Name the blood parasite species.
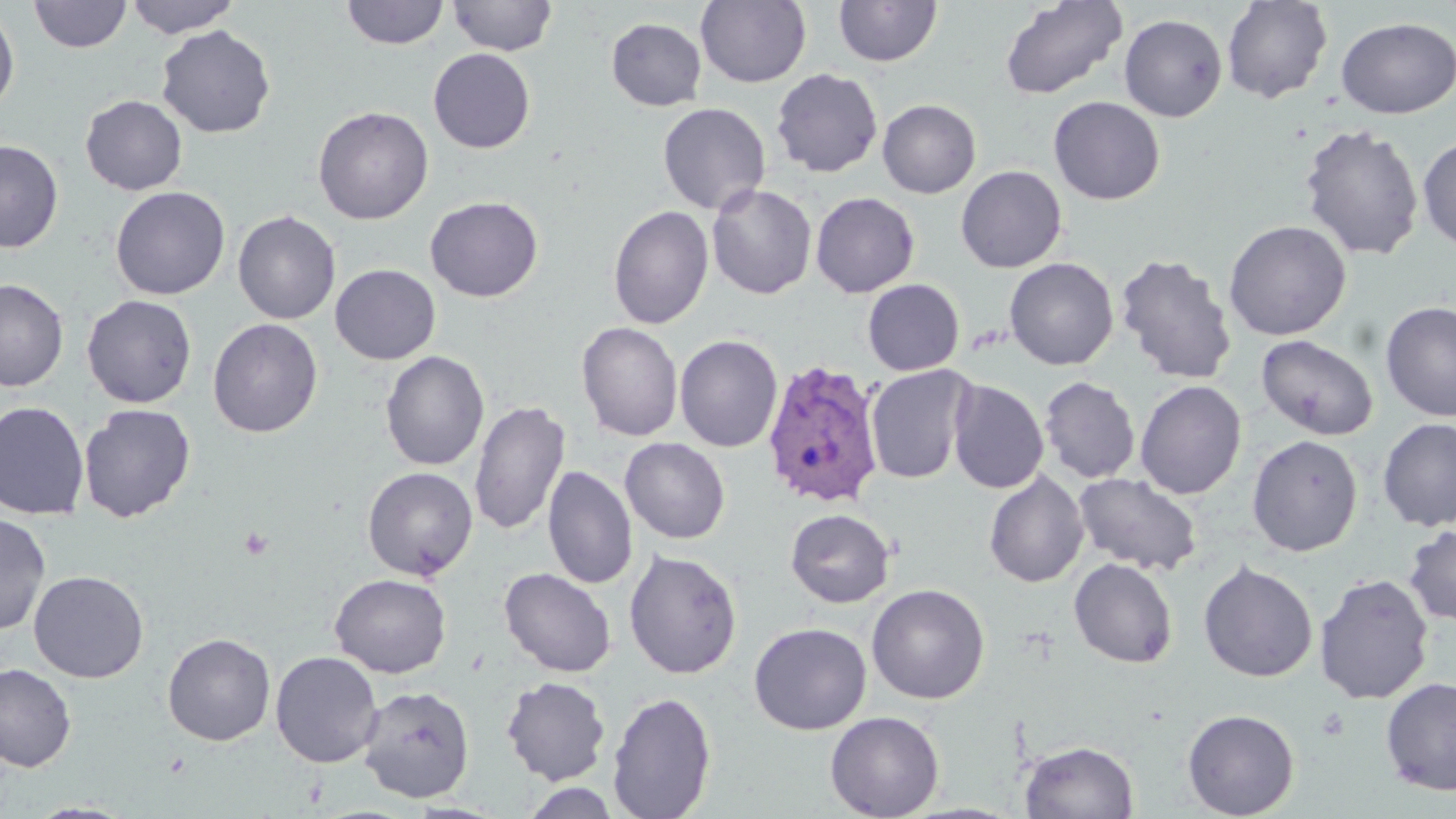

Plasmodium vivax.

image_size: 1456×819 pixels
stain: May-Grünwald-Giemsa
field_of_view: one of a larger specimen
plasmodium_vivax_infected_red_blood_cell_locations: 'approximate bounding boxes as [x1, y1, x2, y2] in pixels: [760, 361, 887, 509]'
uninfected_red_blood_cell_locations: 'approximate bounding boxes as [x1, y1, x2, y2] in pixels: [124, 0, 240, 38], [448, 0, 557, 56], [998, 0, 1129, 100], [1221, 0, 1334, 104], [29, 1, 132, 53], [341, 1, 449, 49], [695, 1, 812, 88], [833, 1, 942, 67], [0, 5, 20, 118], [1220, 9, 1453, 108], [1118, 13, 1227, 122], [1335, 16, 1456, 119], [605, 17, 707, 111], [156, 25, 276, 138], [428, 48, 536, 153], [771, 68, 883, 178], [80, 94, 188, 196], [1048, 96, 1165, 205], [877, 99, 981, 198], [657, 102, 771, 216], [313, 105, 434, 225], [1298, 123, 1425, 261], [1417, 136, 1456, 253], [0, 140, 63, 253], [955, 164, 1067, 273], [706, 183, 817, 299], [110, 186, 230, 300], [810, 192, 920, 297], [425, 195, 544, 302], [607, 205, 714, 330], [232, 210, 341, 324], [1223, 219, 1352, 341], [1115, 252, 1238, 385], [1004, 257, 1119, 371], [330, 263, 441, 365], [0, 278, 69, 391], [862, 279, 965, 376], [82, 294, 197, 408], [1379, 301, 1456, 422], [208, 317, 323, 438], [576, 322, 683, 442], [675, 334, 784, 453], [1255, 334, 1379, 441], [381, 350, 489, 471], [865, 365, 975, 484], [1039, 376, 1140, 484], [947, 379, 1049, 494], [1135, 380, 1247, 499], [469, 399, 570, 537], [0, 401, 90, 520], [78, 403, 196, 523], [1377, 417, 1456, 532], [1247, 434, 1363, 556], [620, 437, 730, 544], [543, 465, 638, 590], [362, 466, 479, 581], [983, 470, 1089, 588], [1073, 472, 1202, 576], [784, 508, 895, 608], [0, 513, 51, 635], [1403, 524, 1456, 627], [624, 548, 743, 679], [1068, 557, 1179, 668], [1198, 560, 1319, 683], [499, 567, 616, 677], [29, 569, 149, 683], [329, 573, 452, 678], [1313, 573, 1434, 705], [866, 583, 990, 705], [748, 622, 872, 735], [162, 632, 276, 746], [270, 650, 384, 768], [0, 662, 77, 772], [1379, 675, 1456, 796], [501, 676, 611, 785], [357, 685, 475, 803], [606, 691, 716, 818], [1182, 708, 1300, 818], [825, 710, 945, 819], [1020, 741, 1139, 819], [521, 783, 622, 819], [25, 801, 137, 819]'
magnification: 1000x
preparation: thin blood smear
modality: light microscopy
platelet_locations: 'approximate bounding boxes as [x1, y1, x2, y2] in pixels: [238, 526, 274, 561]'